Point out each leukocyte.
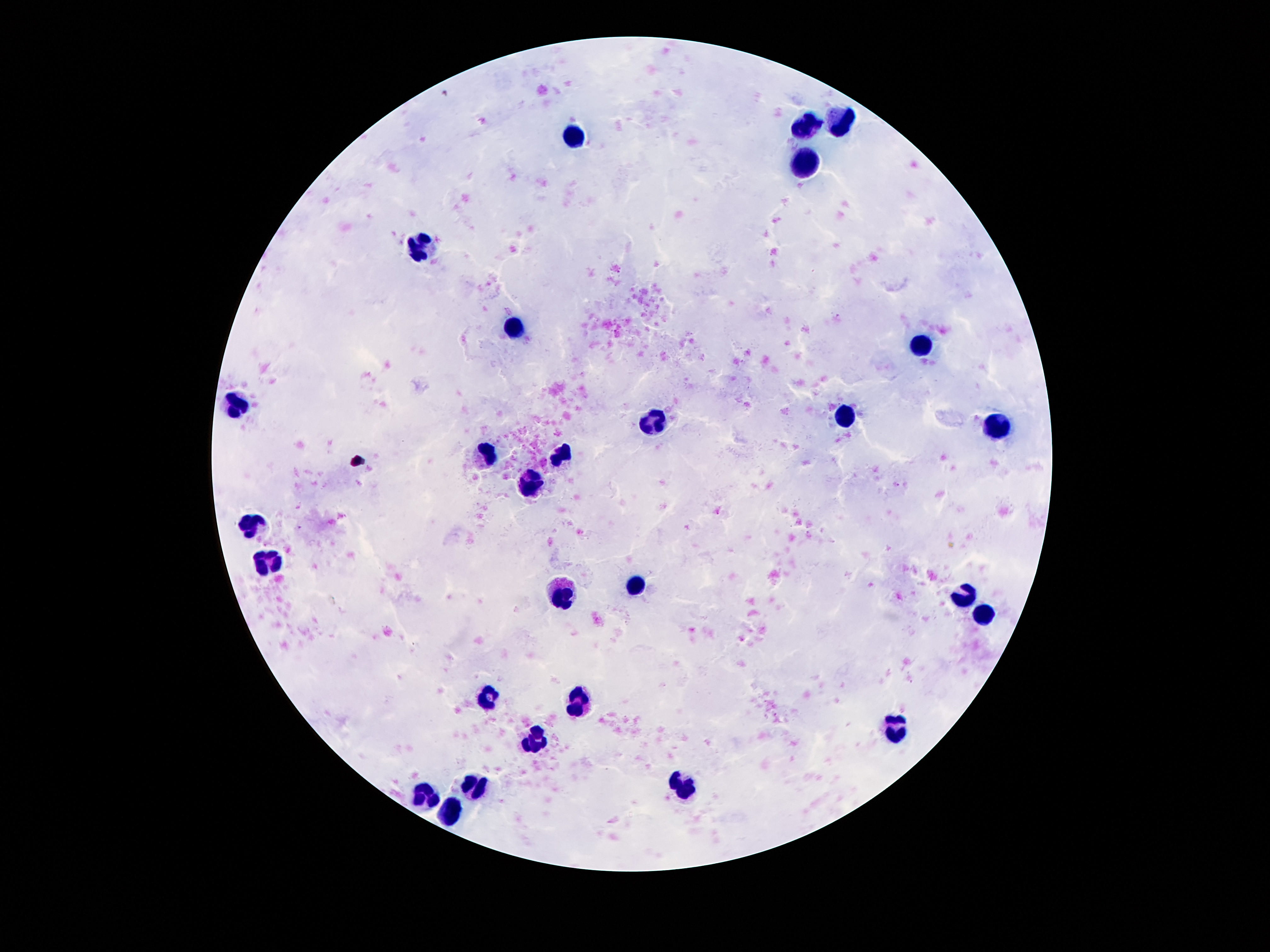
Approximate centers as [x, y] in pixels.
Leukocytes: [842, 118], [803, 127], [577, 134], [803, 163], [420, 245], [510, 327], [920, 343], [235, 404], [844, 419], [650, 420], [999, 429], [489, 454], [562, 456], [534, 482], [256, 526], [269, 563], [637, 585], [562, 591], [963, 593], [986, 618], [487, 700], [579, 703], [900, 731], [534, 741], [476, 786], [683, 787], [427, 800], [452, 813].

patient malaria status = uninfected
stain = Giemsa
capture = smartphone camera through the microscope eyepiece
magnification = 100x
image size = 1270×952 pixels
field of view = single
preparation = thick peripheral-blood smear